Assess this cell for malaria.
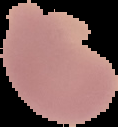
It is uninfected.

image type = cell region segmented out of the field of view; surrounding area masked to black
preparation = thin blood film
image size = 118×127 pixels